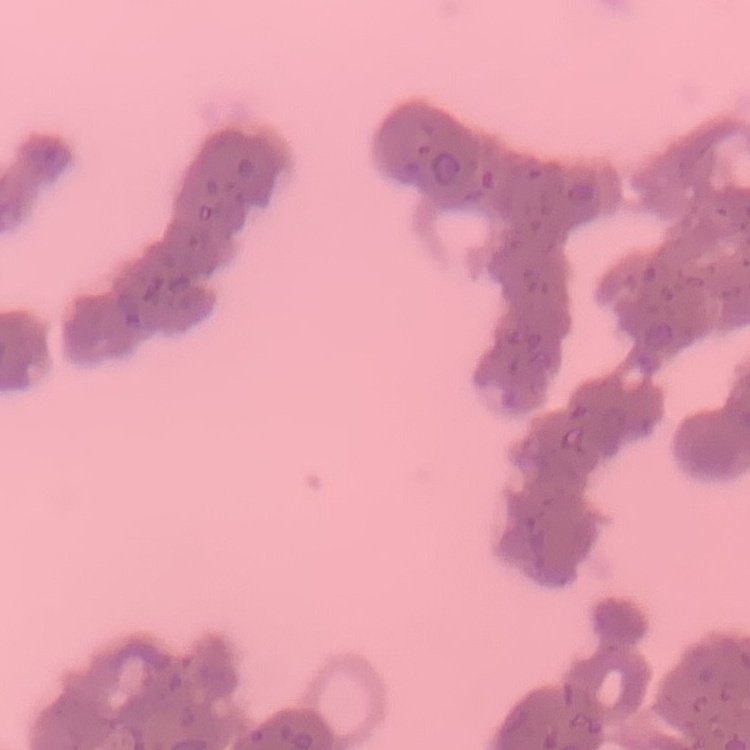

{
  "erythrocyte_morphology": "rouleaux formation",
  "image_type": "square crop of a larger photomicrograph",
  "preparation": "thin peripheral smear",
  "stain": "Field's or Giemsa"
}